Locate and identify every blood parasite.
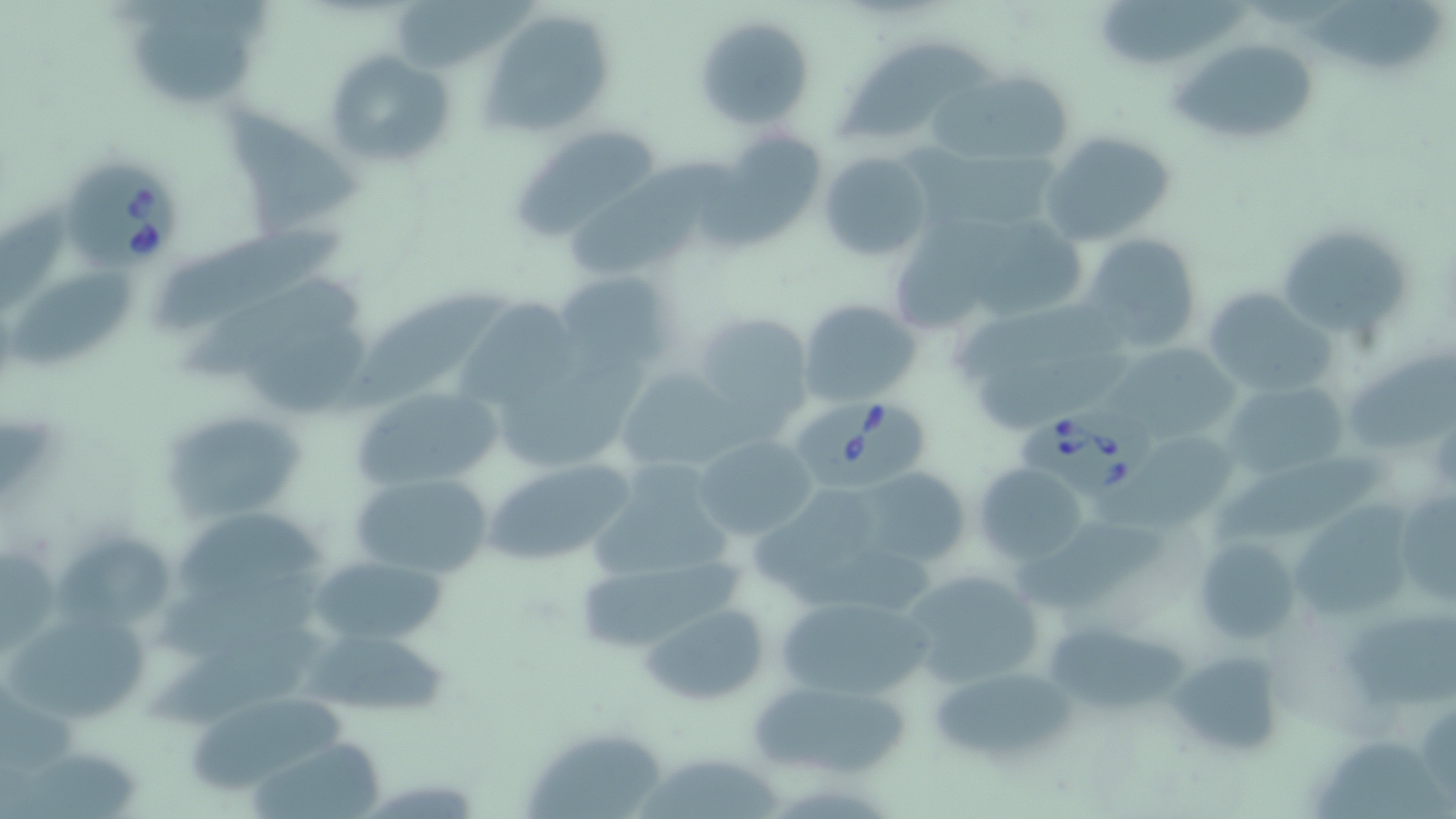

Approximate bounding boxes as (x1, y1, x2, y2) in pixels.
Babesia divergens-infected red blood cells: (58, 159, 181, 270), (798, 396, 932, 487), (1022, 403, 1155, 496).
No Plasmodium falciparum, Plasmodium ovale, Plasmodium malariae, Plasmodium vivax, or Trypanosoma brucei observed.

Uninfected red blood cell locations: (1306, 0, 1448, 76), (397, 1, 536, 71), (1098, 1, 1256, 64), (480, 8, 618, 138), (133, 9, 259, 103), (692, 14, 814, 131), (1174, 37, 1319, 147), (841, 42, 999, 143), (322, 49, 455, 170), (952, 69, 1077, 173), (221, 99, 366, 235), (512, 125, 667, 241), (1039, 129, 1177, 249), (716, 130, 829, 239), (817, 151, 933, 262), (562, 157, 725, 276), (890, 209, 1023, 334), (973, 212, 1089, 319), (1274, 223, 1412, 339), (162, 232, 347, 330), (1080, 233, 1205, 351), (11, 267, 135, 367), (552, 271, 675, 376), (186, 280, 370, 378), (1202, 289, 1334, 397), (339, 292, 503, 408), (457, 294, 568, 417), (798, 299, 919, 405), (692, 309, 816, 438), (231, 316, 371, 417), (972, 336, 1142, 436), (1117, 344, 1248, 442), (1351, 355, 1455, 450), (618, 366, 740, 476), (1226, 379, 1348, 478), (349, 384, 502, 494), (157, 405, 310, 522), (1132, 430, 1238, 524), (692, 433, 818, 542), (1207, 452, 1386, 544), (482, 456, 639, 567), (590, 456, 739, 589), (975, 464, 1089, 563), (854, 467, 970, 568), (352, 471, 494, 580), (1393, 482, 1456, 607), (748, 483, 882, 591), (1290, 497, 1410, 629), (176, 511, 331, 599), (1014, 515, 1178, 601), (55, 534, 172, 633), (1193, 537, 1300, 643), (311, 553, 451, 649), (578, 562, 748, 653), (898, 566, 1046, 691), (775, 594, 931, 702), (643, 604, 768, 706), (7, 613, 150, 724), (1338, 613, 1456, 709), (1044, 623, 1192, 716), (150, 627, 340, 731), (303, 633, 461, 721), (1168, 648, 1285, 759), (926, 664, 1075, 766), (748, 680, 911, 779), (193, 692, 362, 796), (524, 727, 668, 819), (1318, 731, 1456, 819), (245, 734, 394, 818), (639, 760, 783, 819). Slide-level diagnosis: Babesia divergens. Thin blood smear. May-Grünwald-Giemsa stain. Optical microscopy. One field of a larger specimen. Image is 1456×819 pixels. Captured at 1000x magnification.